Report the malaria status of this cell.
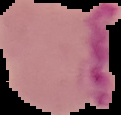

It is parasitized.

preparation = thin blood smear
image type = segmented cell region with the area outside set to black
image size = 121×115 pixels